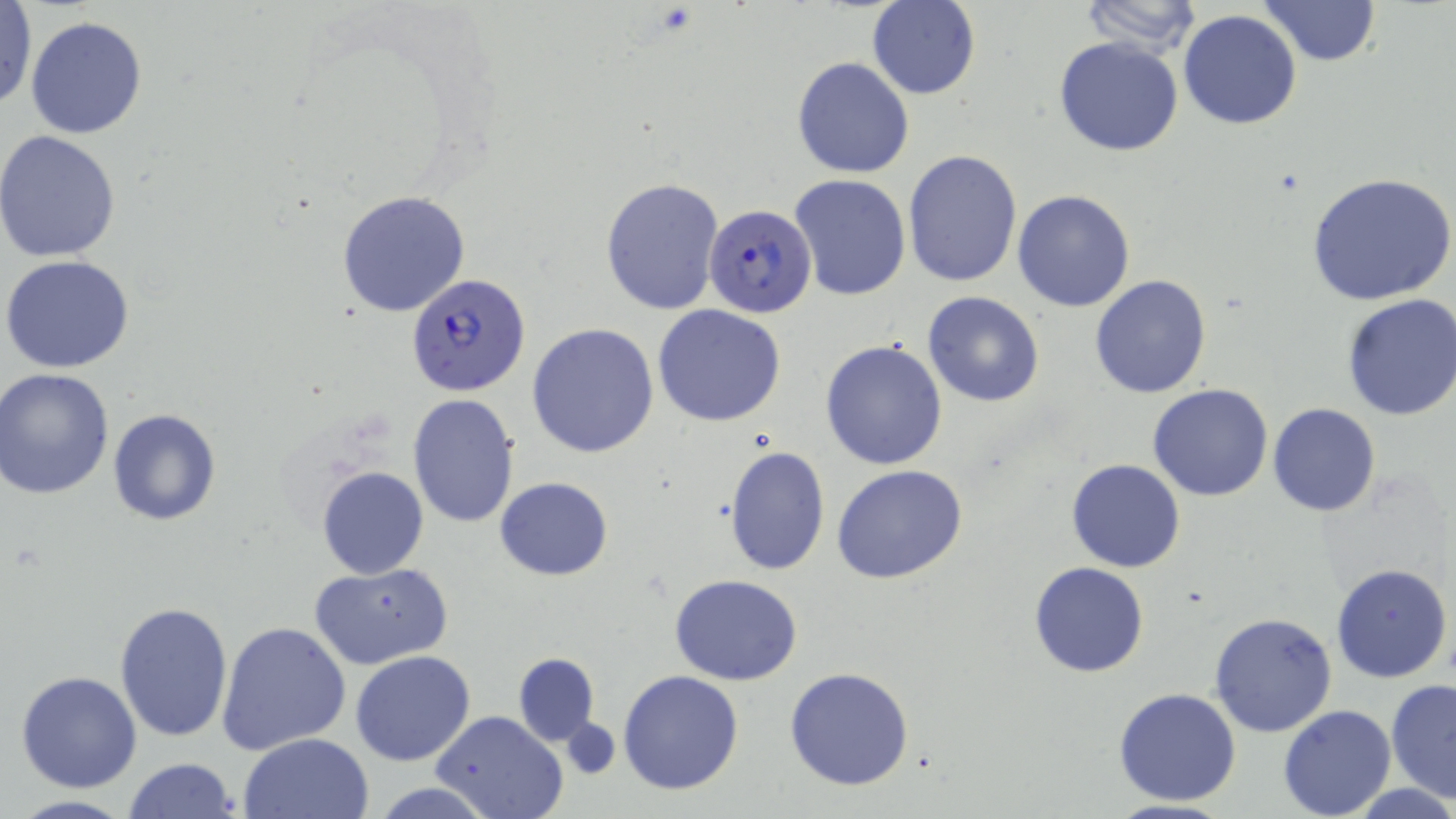
Summary:
  - Coordinate format: approximate bounding boxes as [x1, y1, x2, y2] in pixels
  - Plasmodium falciparum-infected red blood cell locations: [702, 204, 815, 319], [408, 273, 531, 398]
  - Uninfected red blood cell locations: [1078, 0, 1205, 55], [1257, 0, 1382, 67], [867, 1, 980, 101], [0, 3, 35, 109], [1178, 9, 1303, 129], [25, 17, 147, 138], [1053, 36, 1185, 156], [791, 56, 913, 178], [0, 131, 121, 262], [903, 149, 1022, 288], [1307, 171, 1456, 307], [790, 173, 910, 300], [601, 176, 725, 318], [336, 190, 473, 319], [1013, 190, 1137, 312], [3, 255, 136, 373], [1089, 274, 1212, 398], [922, 292, 1045, 408], [1341, 293, 1456, 421], [652, 304, 787, 426], [527, 322, 659, 458], [821, 340, 948, 469], [2, 369, 117, 500], [1148, 383, 1274, 501], [408, 395, 519, 526], [1267, 403, 1381, 517], [107, 409, 224, 526], [723, 445, 830, 576], [1064, 459, 1185, 573], [833, 464, 967, 585], [316, 466, 430, 579], [494, 476, 615, 579], [1028, 562, 1148, 678], [1331, 562, 1452, 683], [310, 563, 453, 672], [670, 574, 803, 686], [114, 601, 233, 743], [1208, 611, 1337, 739], [218, 622, 352, 754], [351, 649, 475, 765], [513, 653, 600, 744], [785, 667, 913, 791], [15, 670, 142, 792], [618, 670, 744, 795], [1385, 677, 1456, 805], [1113, 687, 1241, 806], [1278, 703, 1397, 819], [430, 711, 569, 819], [557, 719, 620, 780], [238, 732, 373, 818], [122, 757, 240, 819], [371, 780, 494, 819], [4, 795, 140, 819], [1099, 799, 1243, 819]
  - Slide-level diagnosis: Plasmodium falciparum
  - Modality: optical microscopy
  - Preparation: thin blood film
  - Stain: May-Grünwald-Giemsa
  - Image size: 1456×819 pixels
  - Magnification: 1000x
  - Field of view: single